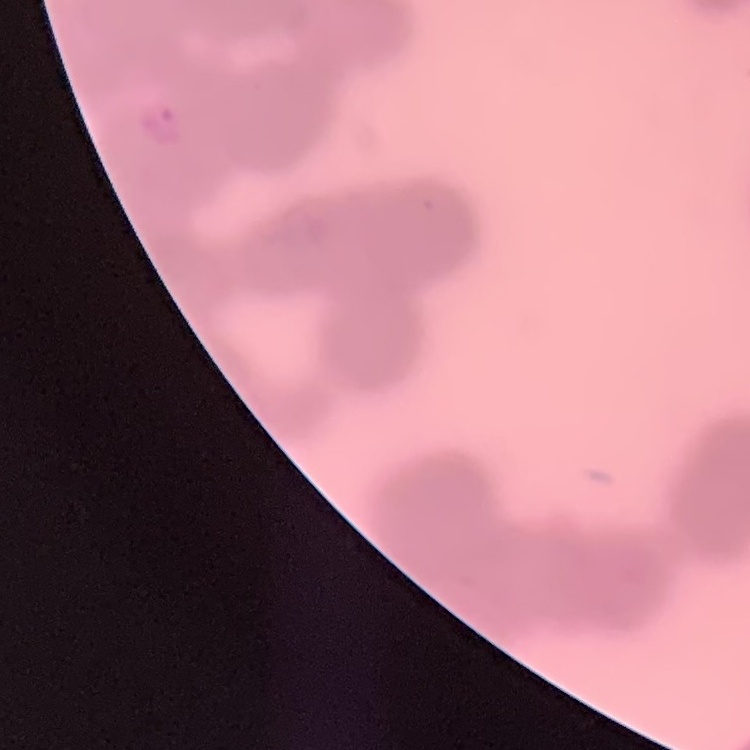

red_blood_cell_morphology: rouleaux formation
image_type: square crop of a larger photomicrograph
preparation: thin peripheral smear
stain: Field's or Giemsa